Classify this cell by malaria status.
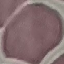

Uninfected.

Summary:
  - Capture: smartphone camera at the microscope eyepiece
  - Stain: Giemsa
  - Image type: cell patch, automatically extracted from a larger field of view and resized to 64 × 64 pixels
  - Preparation: thin blood smear